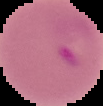 Segmented cell region on a black background. From a thin blood film. Image is 103×106 pixels. Result: Plasmodium parasites identified.